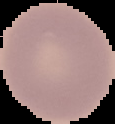

{
  "image_type": "segmented cell region on a black background",
  "image_size": "115×124 pixels",
  "malaria_status": "uninfected",
  "preparation": "thin blood film"
}